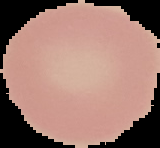 Cell region segmented out of the field of view; the surrounding area is masked to black. From a thin blood film. Malaria status: uninfected. Image is 160×148 pixels.